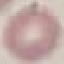

result = no malaria parasites detected
image type = cell patch, automatically extracted from a larger field of view and resized to 64 × 64 pixels
stain = Giemsa
capture = smartphone camera at the microscope eyepiece
preparation = thin blood film